Assess the morphology of the red blood cells.
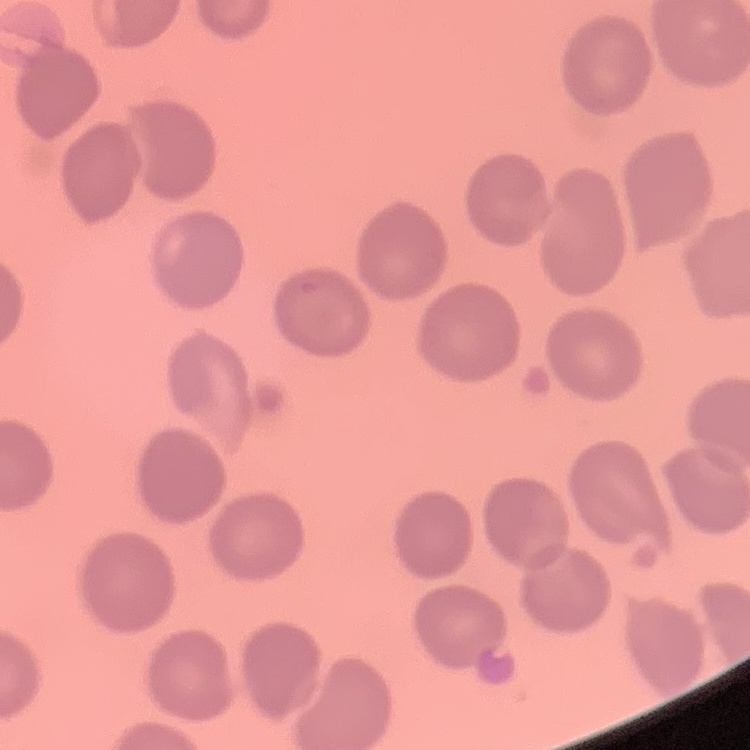
They show no rouleaux formation.

Square crop of a larger photomicrograph. Thin blood film. Field's or Giemsa stain.